Identify the parasite.
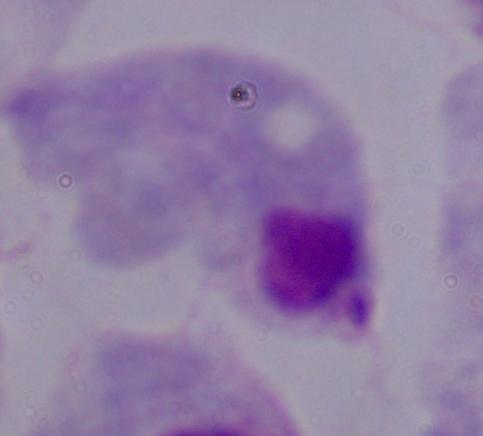

This is a trichomonad.

magnification: 1000x
modality: photomicrograph